Assess this cell for malaria.
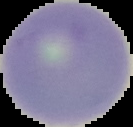
Uninfected.

Image is 133×127 pixels. From a thin blood film. Segmented cell region on a black background.